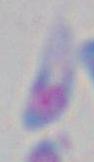
identification = Toxoplasma gondii
magnification = 1000x
modality = photomicrograph